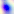

Summary:
  - Magnification: 400x
  - Modality: photomicrograph
  - Identification: Toxoplasma gondii